Assess for malaria.
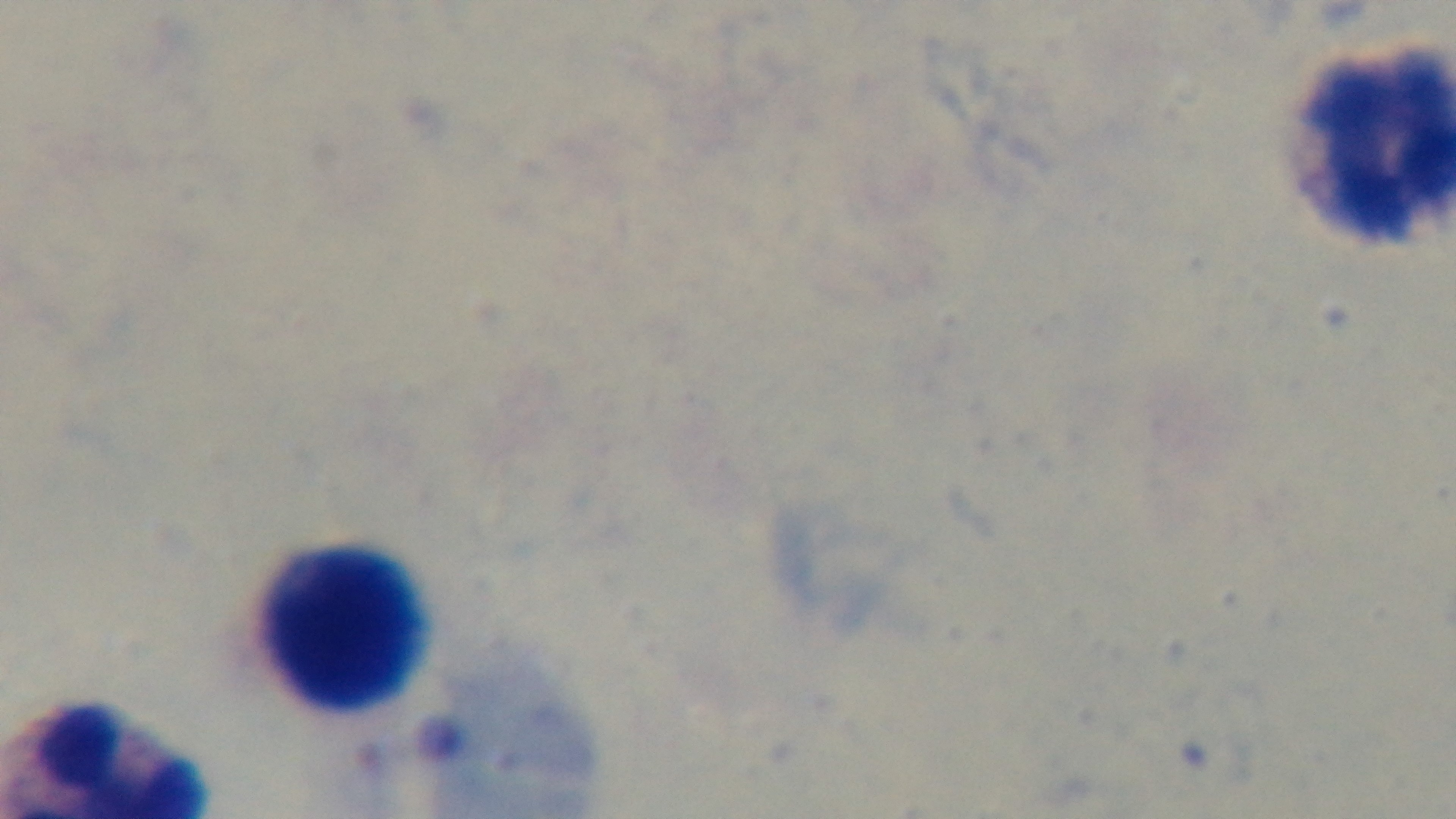

Uninfected.

Summary:
  - Objective: 100x oil immersion
  - Preparation: thick
  - Modality: light microscopy
  - Stain: Giemsa
  - Capture: mounted 4K digital camera
  - Field of view: one from the slide